Locate and identify every blood parasite.
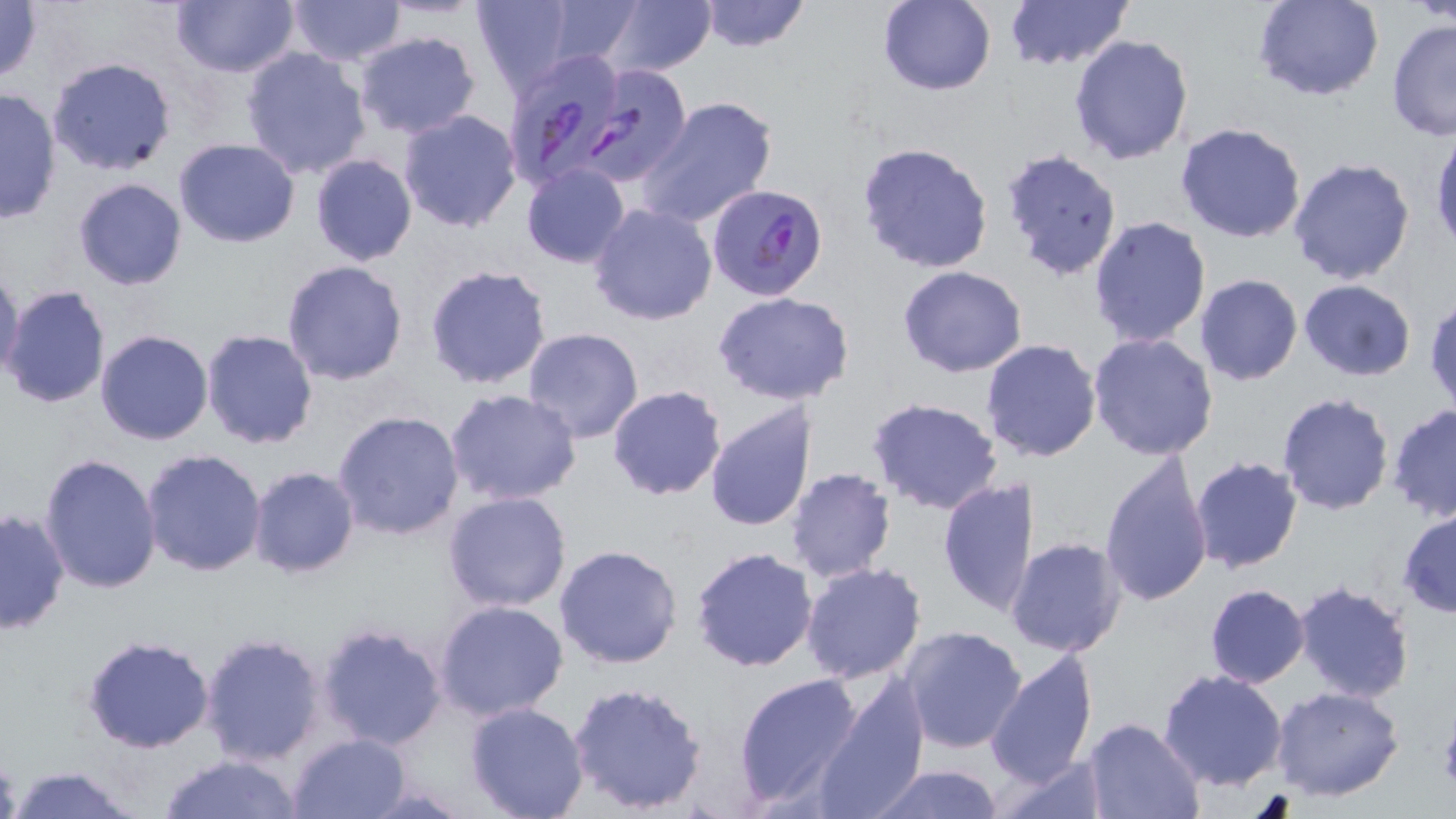
Approximate bounding boxes as [x1, y1, x2, y2] in pixels.
Plasmodium falciparum-infected red blood cells: [501, 50, 630, 191], [579, 62, 691, 185], [707, 181, 829, 305].
No Plasmodium ovale, Plasmodium malariae, Plasmodium vivax, Babesia divergens, or Trypanosoma brucei observed.

{
  "slide_level_diagnosis": "Plasmodium falciparum",
  "magnification": "1000x",
  "uninfected_red_blood_cell_locations": "approximate bounding boxes as [x1, y1, x2, y2] in pixels: [0, 0, 45, 85], [169, 0, 301, 79], [286, 0, 404, 65], [470, 0, 577, 95], [604, 0, 715, 76], [698, 0, 811, 53], [1004, 0, 1133, 71], [1413, 0, 1455, 25], [538, 1, 645, 68], [879, 1, 997, 96], [1253, 1, 1385, 101], [1386, 18, 1456, 141], [354, 30, 481, 137], [1068, 34, 1194, 165], [240, 46, 372, 178], [47, 56, 178, 175], [0, 87, 62, 226], [638, 96, 778, 228], [398, 109, 522, 233], [1175, 122, 1308, 243], [1430, 128, 1456, 255], [174, 137, 300, 247], [856, 140, 994, 275], [1001, 146, 1124, 281], [309, 153, 417, 266], [1287, 156, 1416, 285], [520, 164, 631, 268], [72, 178, 189, 291], [587, 202, 717, 326], [1087, 215, 1213, 348], [281, 260, 410, 386], [424, 264, 552, 390], [1, 265, 24, 382], [898, 266, 1026, 378], [1194, 273, 1303, 385], [1298, 279, 1416, 381], [2, 284, 112, 410], [919, 284, 1070, 406], [712, 291, 856, 405], [1426, 295, 1456, 415], [200, 328, 319, 450], [521, 328, 646, 445], [96, 329, 213, 445], [1087, 333, 1219, 461], [987, 338, 1105, 463], [606, 385, 726, 500], [445, 389, 582, 507], [1277, 393, 1397, 516], [865, 398, 1005, 515], [703, 399, 818, 532], [1387, 404, 1456, 523], [332, 410, 465, 542], [141, 448, 269, 576], [1100, 452, 1214, 608], [40, 454, 162, 595], [1189, 456, 1304, 573], [247, 466, 360, 578], [787, 468, 898, 583], [937, 476, 1035, 617], [442, 491, 571, 612], [0, 508, 69, 634], [1397, 508, 1456, 618], [1008, 536, 1127, 657], [554, 543, 683, 669], [690, 546, 819, 672], [801, 562, 926, 684], [1293, 579, 1416, 703], [1203, 584, 1309, 688], [434, 599, 568, 721], [317, 622, 449, 751], [900, 625, 1027, 754], [199, 631, 328, 764], [82, 635, 215, 754], [985, 647, 1099, 787], [1157, 669, 1289, 791], [733, 671, 866, 808], [807, 679, 930, 819], [567, 680, 709, 815], [1272, 685, 1404, 801], [465, 703, 590, 819], [1081, 717, 1203, 818], [287, 732, 410, 818], [159, 753, 308, 819], [994, 754, 1110, 819], [867, 764, 1007, 818], [8, 765, 143, 819]",
  "field_of_view": "single",
  "modality": "light microscopy",
  "preparation": "thin blood smear",
  "stain": "May-Grünwald-Giemsa",
  "platelet_locations": "approximate bounding boxes as [x1, y1, x2, y2] in pixels: [1438, 715, 1456, 791]",
  "image_size": "1456×819 pixels"
}